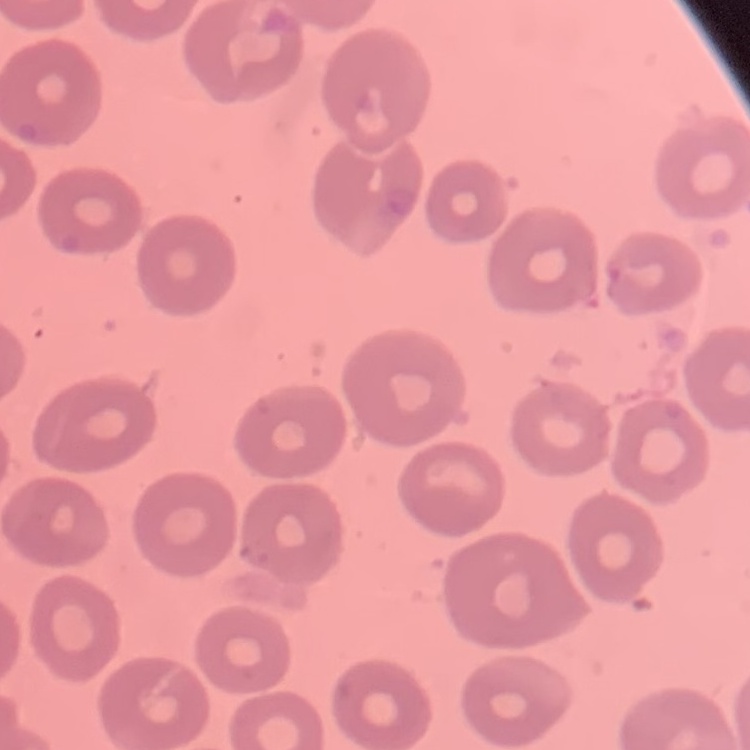
The erythrocytes show no rouleaux formation. Thin blood smear. Square crop of a larger photomicrograph. Stained with either Field's or Giemsa.